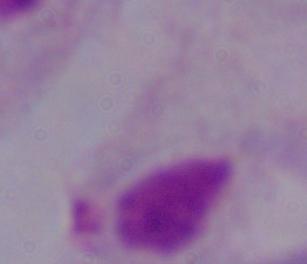

identification: trichomonad
modality: photomicrograph
magnification: 1000x